Name the blood parasite species.
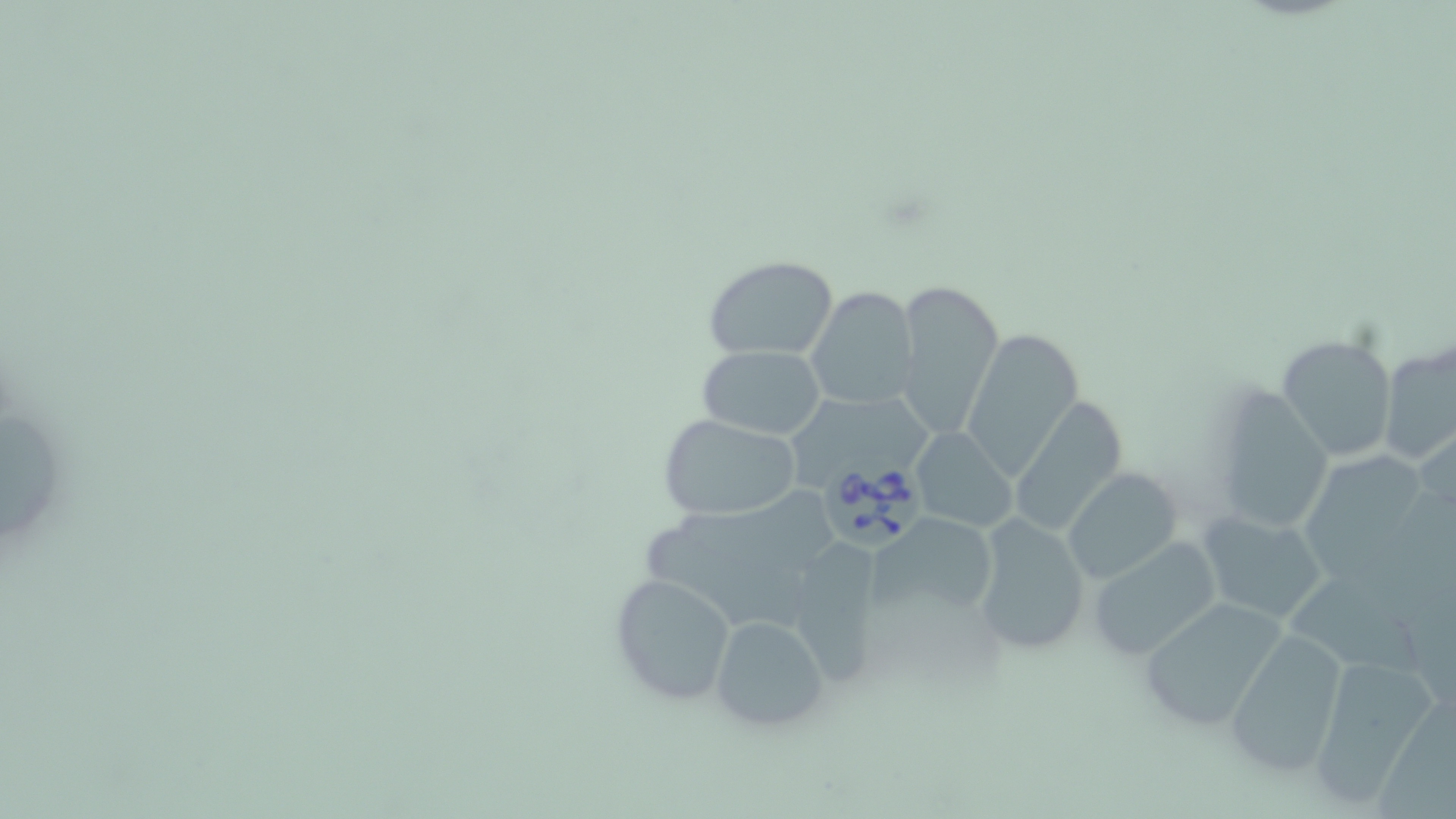
Babesia divergens.

preparation: thin blood film
uninfected_red_blood_cell_locations: 'approximate bounding boxes as (x1,y1)-(x2,y2) corner pairs in pixels: (703,254)-(839,361), (893,277)-(1005,441), (805,285)-(916,409), (961,326)-(1085,473), (1274,334)-(1397,462), (1379,341)-(1455,465), (698,345)-(826,441), (1209,384)-(1333,540), (796,395)-(939,491), (1011,399)-(1132,534), (659,414)-(801,521), (908,428)-(1018,531), (1305,454)-(1421,581), (1063,469)-(1181,583), (870,509)-(1000,626), (1195,509)-(1327,626), (971,513)-(1092,657), (798,538)-(880,688), (1087,538)-(1222,663), (1291,570)-(1430,693), (610,572)-(739,706), (1136,596)-(1290,732), (707,613)-(831,733), (1226,631)-(1351,779), (1306,652)-(1444,806)'
field_of_view: one of a larger specimen
babesia_divergens_infected_red_blood_cell_locations: 'approximate bounding boxes as (x1,y1)-(x2,y2) corner pairs in pixels: (814,451)-(930,553)'
stain: May-Grünwald-Giemsa
modality: optical microscopy
image_size: 1456×819 pixels
magnification: 1000x